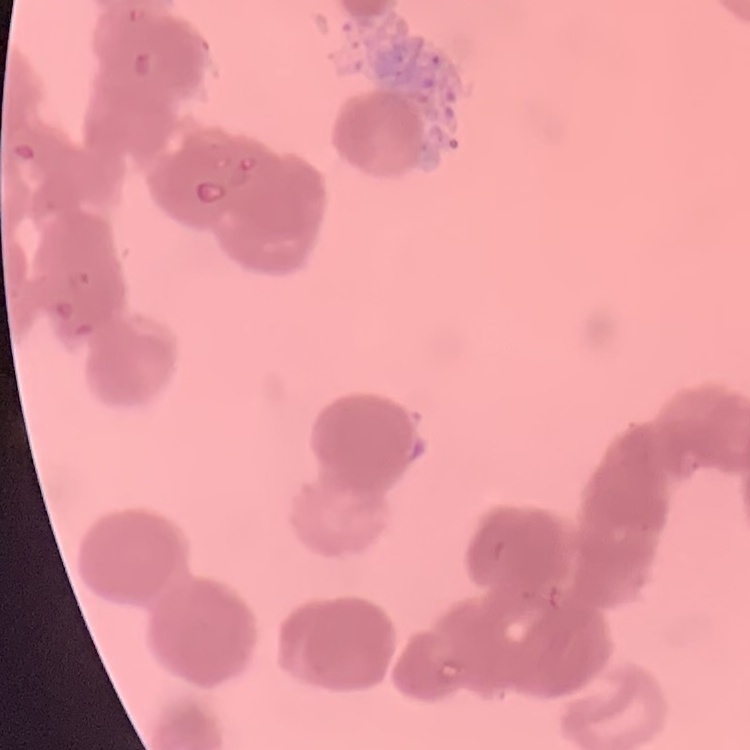
Summary:
  - Red blood cell morphology: rouleaux formation
  - Preparation: thin peripheral smear
  - Image type: square crop of a larger photomicrograph
  - Stain: Field's or Giemsa